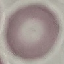
result = negative for malaria parasites
image type = cell patch, automatically extracted from a larger field of view and resized to 64 × 64 pixels
stain = Giemsa
preparation = thin blood film
capture = smartphone through the microscope eyepiece